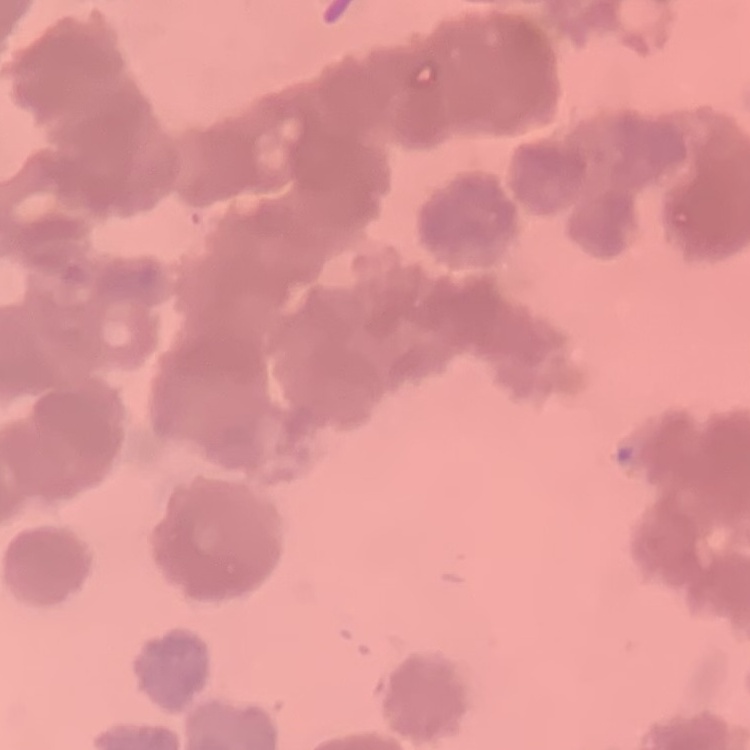
red_blood_cell_morphology: rouleaux formation
stain: Field's or Giemsa
preparation: thin blood film
image_type: square crop of a larger photomicrograph